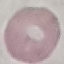

malaria_status: uninfected
stain: Giemsa
image_type: automatically extracted cell patch, resized to 64 × 64 pixels
preparation: thin blood smear
capture: smartphone through the microscope eyepiece